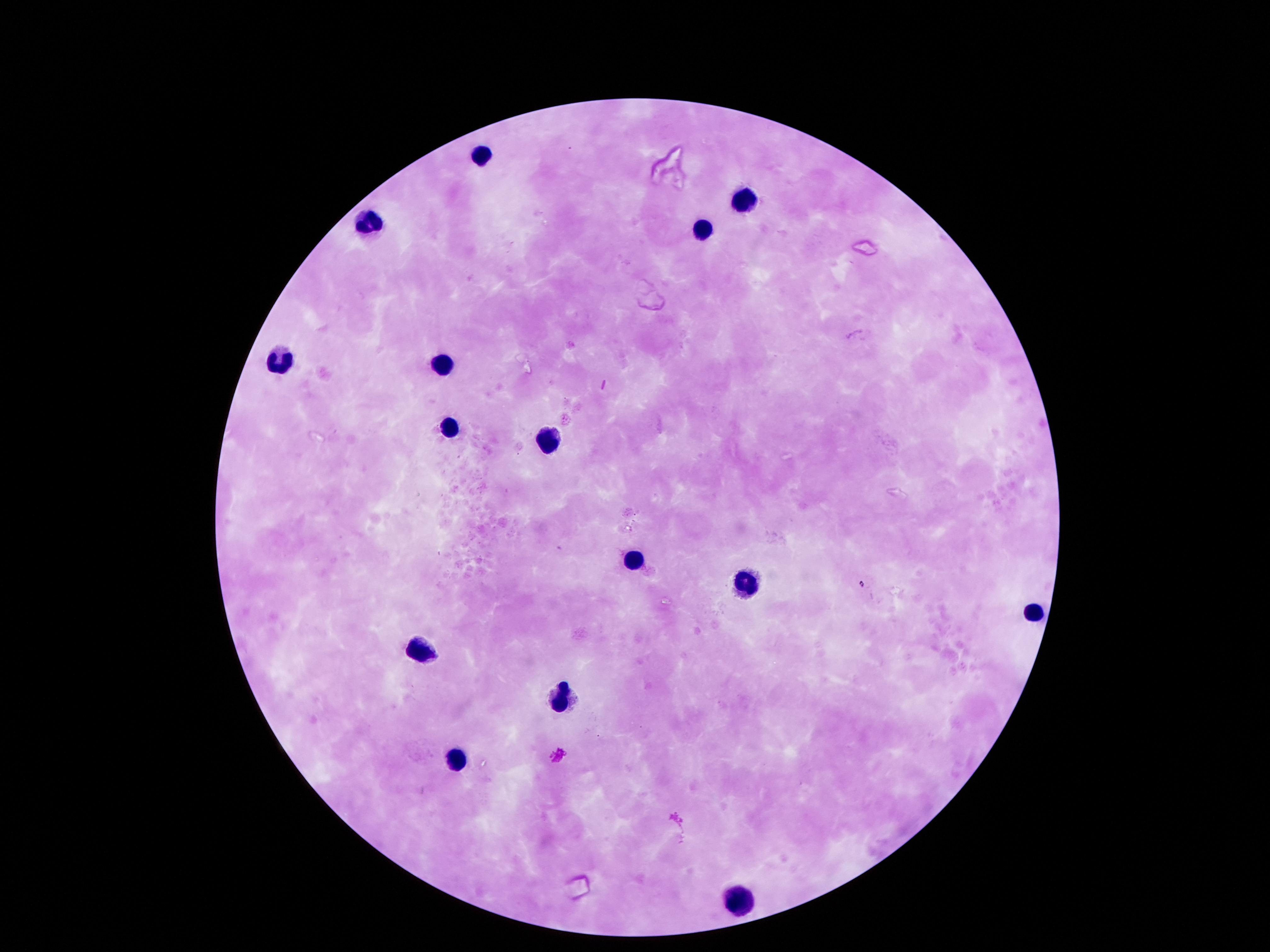
{
  "image_size": "1270×952 pixels",
  "preparation": "thick blood film",
  "leukocyte_locations": "approximate centers as {x, y} in pixels: {484, 154}, {742, 193}, {367, 220}, {700, 228}, {442, 358}, {280, 361}, {451, 425}, {551, 436}, {632, 558}, {745, 574}, {1033, 610}, {419, 649}, {564, 688}, {451, 759}, {742, 897}",
  "stain": "Giemsa",
  "field_of_view": "single",
  "magnification": "100x",
  "patient_malaria_status": "negative",
  "capture": "smartphone camera through the microscope eyepiece"
}